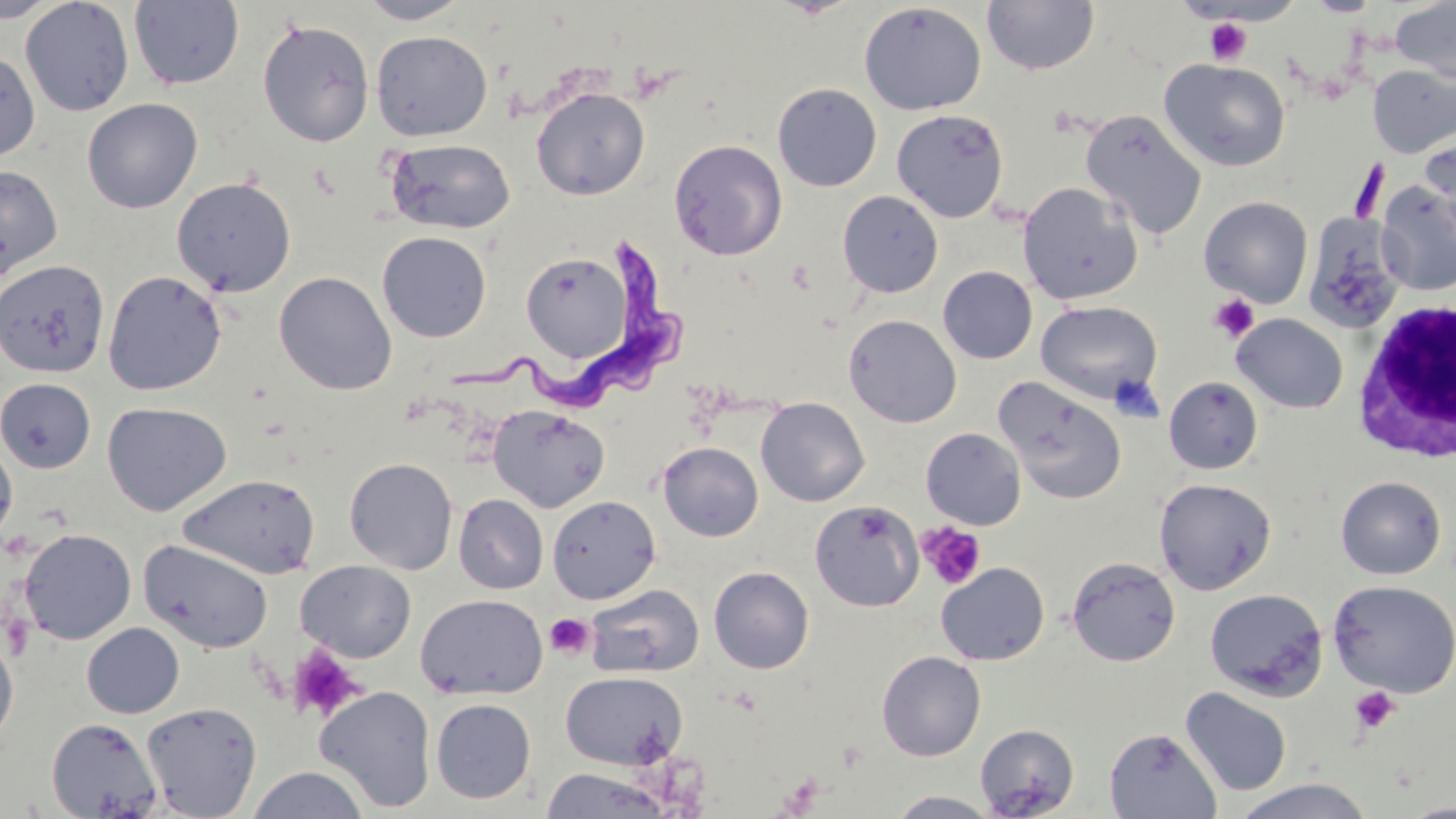
slide-level diagnosis = Trypanosoma brucei
image size = 1456×819 pixels
uninfected red blood cell locations = approximate bounding boxes as (x1, y1, x2, y2) in pixels: (0, 0, 62, 24), (20, 0, 134, 116), (128, 0, 245, 90), (357, 0, 472, 25), (1306, 0, 1380, 17), (982, 1, 1099, 75), (1390, 1, 1456, 83), (859, 2, 986, 115), (257, 18, 375, 147), (370, 30, 493, 141), (0, 48, 40, 163), (1159, 58, 1290, 172), (1367, 64, 1456, 157), (772, 82, 882, 192), (531, 87, 650, 200), (82, 98, 202, 214), (891, 109, 1009, 222), (1080, 109, 1207, 240), (1419, 129, 1456, 239), (384, 138, 516, 235), (669, 139, 788, 261), (0, 165, 62, 281), (171, 176, 296, 297), (1017, 181, 1143, 305), (1375, 181, 1456, 295), (837, 190, 943, 298), (1199, 196, 1314, 308), (1303, 213, 1407, 334), (377, 232, 492, 342), (521, 250, 632, 363), (0, 260, 110, 379), (938, 265, 1038, 364), (102, 270, 227, 396), (274, 270, 397, 395), (1035, 300, 1162, 404), (1231, 313, 1348, 413), (844, 314, 961, 428), (993, 376, 1127, 505), (1164, 376, 1263, 474), (0, 377, 96, 473), (756, 397, 869, 507), (102, 401, 232, 517), (487, 404, 610, 512), (921, 427, 1026, 529), (0, 434, 17, 547), (658, 442, 763, 541), (344, 457, 459, 574), (177, 474, 320, 579), (1335, 475, 1447, 580), (1154, 477, 1276, 595), (453, 494, 549, 594), (547, 495, 661, 604), (809, 500, 923, 612), (19, 528, 137, 644), (138, 539, 274, 654), (1066, 555, 1181, 666), (296, 560, 417, 661), (935, 562, 1050, 666), (708, 566, 814, 674), (1327, 579, 1456, 697), (584, 583, 704, 679), (1204, 589, 1328, 700), (415, 593, 548, 700), (82, 622, 185, 718), (0, 632, 18, 750), (876, 650, 986, 761), (560, 670, 688, 771), (313, 685, 437, 812), (1180, 687, 1292, 797), (430, 698, 536, 804), (142, 701, 262, 818), (46, 717, 163, 818), (975, 724, 1079, 818), (1104, 727, 1221, 818), (247, 766, 370, 819), (539, 767, 673, 818), (1231, 778, 1377, 818), (886, 790, 1001, 818), (1397, 800, 1456, 819)
platelet locations = approximate bounding boxes as (x1, y1, x2, y2) in pixels: (1204, 18, 1252, 65), (1208, 295, 1259, 342), (917, 522, 987, 590), (545, 612, 595, 660), (286, 644, 366, 724), (1349, 687, 1400, 735)
preparation = thin blood film
Trypanosoma brucei locations = approximate bounding boxes as (x1, y1, x2, y2) in pixels: (438, 235, 689, 404)
modality = optical microscopy
magnification = 1000x
field of view = single
white blood cell locations = approximate bounding boxes as (x1, y1, x2, y2) in pixels: (1350, 298, 1455, 462)
stain = May-Grünwald-Giemsa